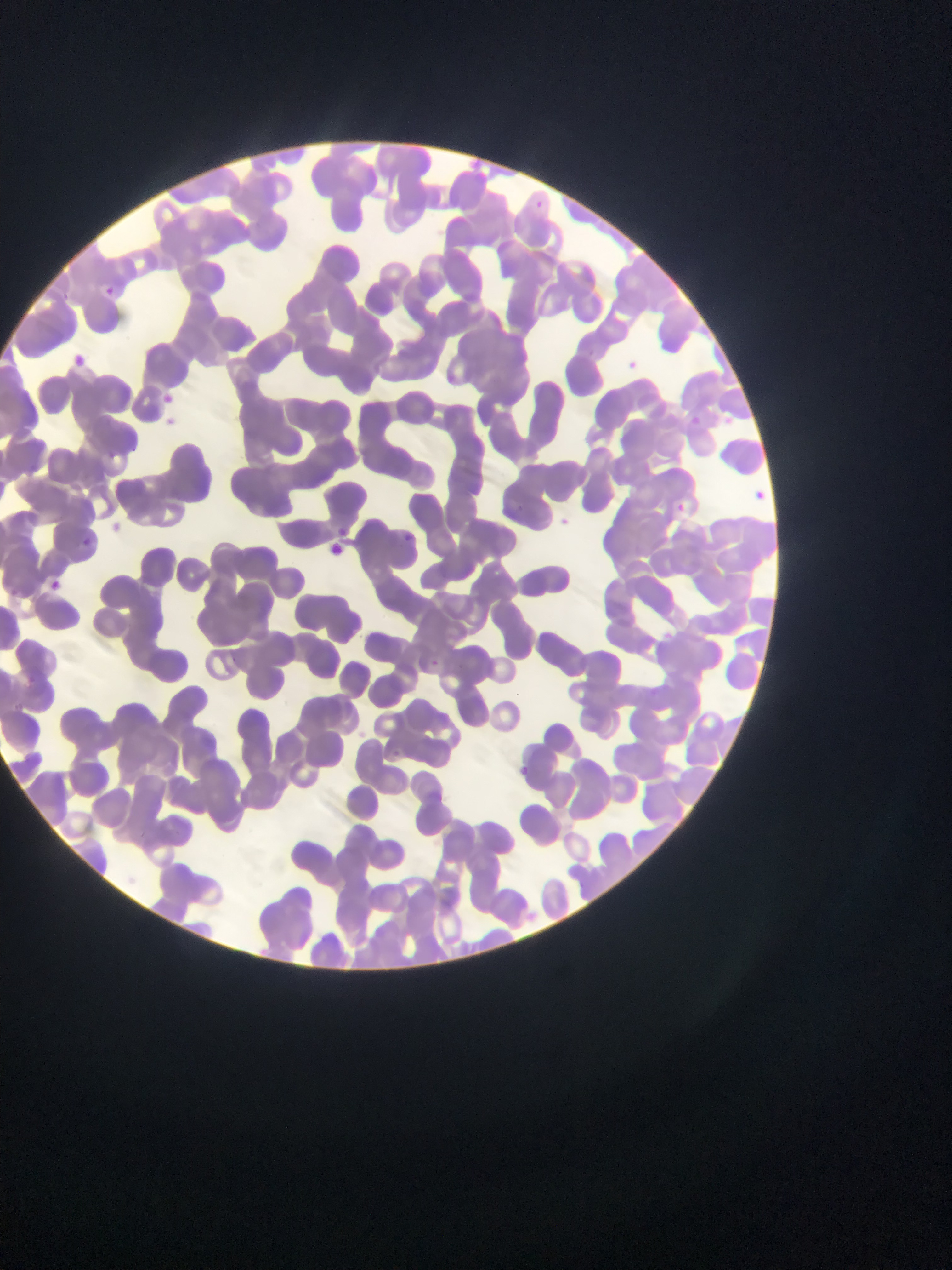
Approximate bounding boxes as (left, top, right, bottom) in pixels.
Summary:
  - Plasmodium parasite locations: (532, 197, 543, 209), (95, 281, 124, 305), (588, 345, 597, 362), (78, 353, 101, 383), (622, 357, 643, 376), (164, 395, 173, 403), (687, 413, 703, 428), (104, 448, 112, 464), (750, 487, 769, 504), (670, 500, 690, 517), (552, 513, 576, 533), (335, 527, 349, 535), (396, 529, 418, 549), (78, 537, 91, 550), (38, 575, 66, 600), (430, 657, 443, 668), (393, 747, 410, 758), (517, 761, 533, 773)
  - Image size: 952×1270 pixels
  - Field of view: single
  - Preparation: thin blood film
  - Country: Ghana
  - Capture: mobile-phone photograph through a microscope